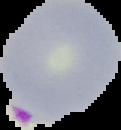

image_type: cell region segmented out of the field of view; surrounding area masked to black
malaria_status: parasitized
preparation: thin blood film
image_size: 121×130 pixels